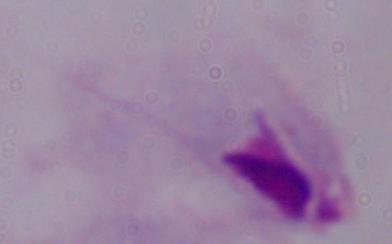
magnification: 1000x
identification: trichomonad
modality: micrograph